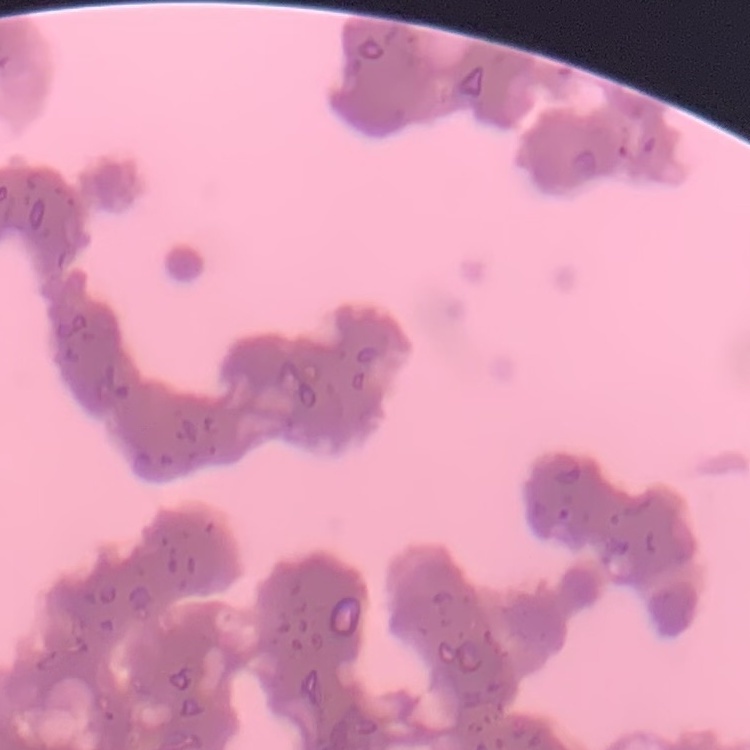 The erythrocytes show rouleaux formation. Thin blood film. Stained with either Field's or Giemsa. One tile cut from a larger photomicrograph.